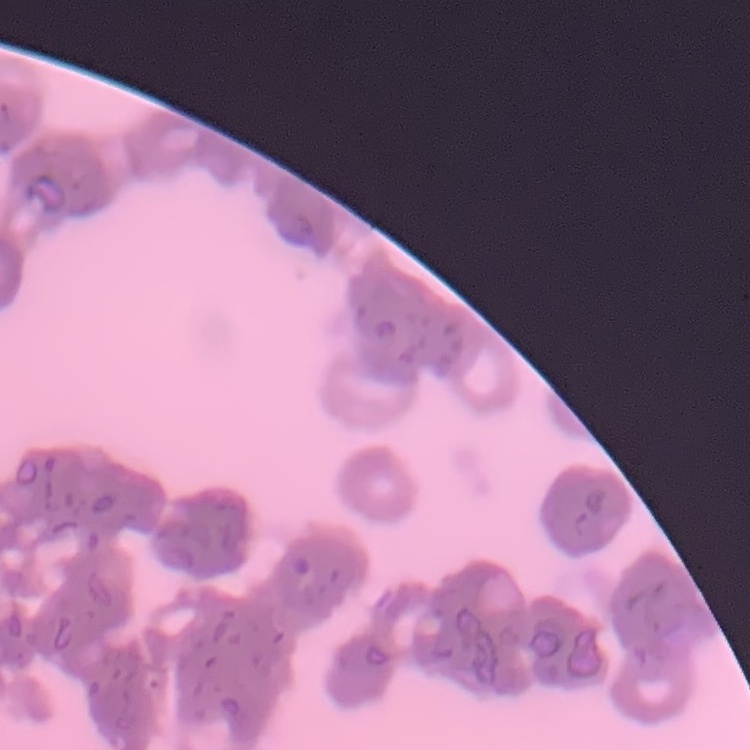 The red blood cells exhibit rouleaux formation. Thin blood film. Square crop of a larger photomicrograph. Field's or Giemsa stain.